Assess this cell for malaria.
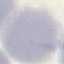
Uninfected.

stain: Giemsa
preparation: thin blood smear
image_type: automatically extracted cell patch, resized to 64 × 64 pixels
capture: smartphone through the microscope eyepiece